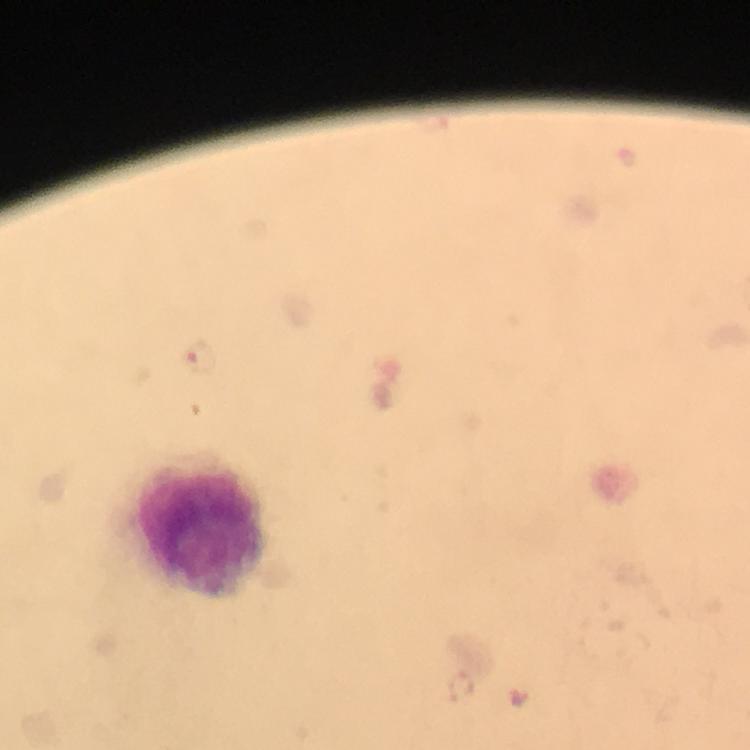

Approximate centers as [x, y] in pixels.
Summary:
  - Leukocyte locations: [204, 530]
  - Malaria parasite locations: [196, 356], [462, 688]
  - Preparation: thick blood smear
  - Cropped from: one field of view
  - Stain: Giemsa
  - Capture: smartphone camera through the microscope
  - Immersion oil: applied
  - Magnification: 100x
  - Image size: 750×750 pixels
  - Context: from a malaria diagnostic workup